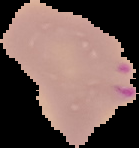 Image is 139×148 pixels. From a thin blood film. Malaria status: parasitized. Cell region segmented out of the field of view; the surrounding area is masked to black.